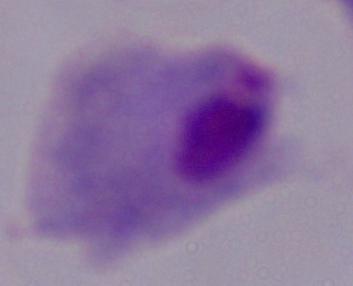
magnification: 1000x
modality: photomicrograph
identification: trichomonad